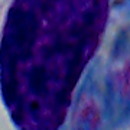
magnification = 1000x
modality = photomicrograph
identification = white blood cell